State which parasite is depicted.
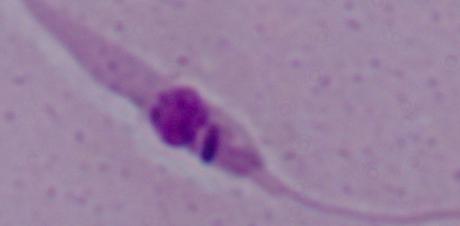

Leishmania.

Summary:
  - Magnification: 1000x
  - Modality: photomicrograph